Outline each Plasmodium falciparum-infected red blood cell.
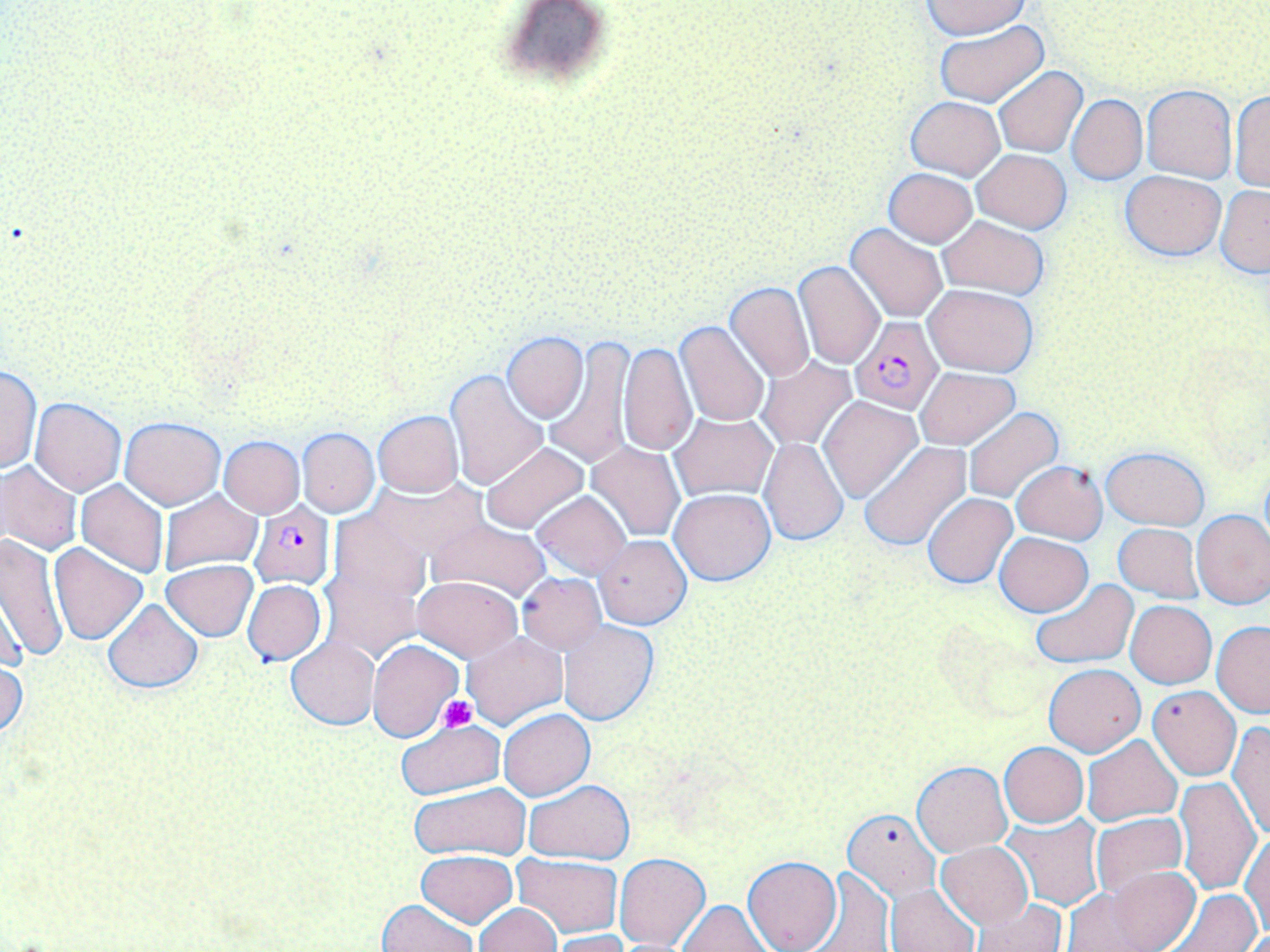
Approximate bounding boxes as [x1, y1, x2, y2] in pixels.
Plasmodium falciparum-infected red blood cells: [850, 316, 944, 413], [249, 502, 335, 590].

slide_level_diagnosis: Plasmodium falciparum
uninfected_red_blood_cell_locations: 'approximate bounding boxes as [x1, y1, x2, y2] in pixels: [924, 1, 1031, 41], [492, 3, 621, 97], [932, 22, 1051, 108], [993, 67, 1088, 157], [1141, 84, 1237, 181], [1229, 90, 1269, 192], [1067, 94, 1147, 184], [907, 96, 1004, 180], [972, 149, 1072, 232], [884, 168, 978, 246], [1120, 170, 1225, 261], [1216, 186, 1269, 277], [938, 215, 1049, 298], [846, 224, 948, 324], [793, 260, 885, 369], [724, 282, 815, 382], [922, 284, 1038, 377], [690, 297, 801, 410], [673, 322, 769, 427], [501, 332, 588, 422], [545, 338, 634, 467], [618, 341, 696, 458], [757, 357, 856, 450], [1, 365, 41, 475], [915, 367, 1018, 450], [445, 370, 548, 491], [819, 395, 922, 502], [30, 398, 126, 495], [962, 406, 1063, 504], [373, 411, 462, 498], [669, 412, 777, 502], [119, 416, 225, 509], [297, 428, 379, 516], [217, 435, 305, 517], [759, 437, 847, 544], [480, 441, 589, 533], [586, 441, 685, 542], [860, 441, 970, 549], [1101, 446, 1208, 529], [1011, 460, 1107, 543], [0, 462, 83, 555], [373, 478, 489, 566], [75, 480, 170, 578], [669, 487, 776, 585], [531, 490, 630, 580], [158, 491, 263, 576], [923, 493, 1017, 589], [326, 509, 431, 613], [1192, 509, 1270, 609], [425, 518, 552, 602], [1113, 523, 1204, 603], [994, 531, 1094, 617], [1, 532, 66, 660], [594, 534, 692, 629], [49, 542, 148, 645], [321, 558, 425, 662], [162, 560, 258, 641], [517, 572, 606, 653], [412, 575, 521, 661], [1030, 577, 1139, 668], [242, 580, 325, 665], [102, 599, 203, 693], [1125, 601, 1217, 689], [557, 620, 658, 725], [1211, 621, 1270, 718], [462, 630, 567, 729], [286, 636, 379, 729], [369, 639, 463, 743], [0, 648, 27, 741], [1043, 664, 1146, 756], [1148, 685, 1241, 780], [499, 709, 593, 801], [395, 718, 505, 798], [1228, 721, 1270, 840], [1083, 735, 1183, 827], [999, 742, 1089, 827], [912, 760, 1012, 855], [1174, 776, 1261, 895], [523, 779, 636, 862], [408, 783, 531, 860], [843, 809, 940, 901], [1090, 814, 1187, 900], [1002, 815, 1105, 910], [1241, 831, 1269, 941], [935, 842, 1032, 929], [416, 850, 517, 927], [613, 852, 710, 951], [511, 853, 622, 938], [742, 856, 842, 952], [1091, 866, 1200, 952], [804, 867, 894, 952], [885, 882, 980, 952], [1059, 886, 1168, 951], [1162, 888, 1264, 952], [376, 899, 478, 952], [678, 900, 771, 951], [969, 900, 1065, 952], [473, 903, 562, 952], [546, 930, 635, 952]'
magnification: 1000x
stain: May-Grünwald-Giemsa
platelet_locations: 'approximate bounding boxes as [x1, y1, x2, y2] in pixels: [438, 695, 476, 732]'
image_size: 1270×952 pixels
modality: light microscopy
field_of_view: single
preparation: thin blood smear